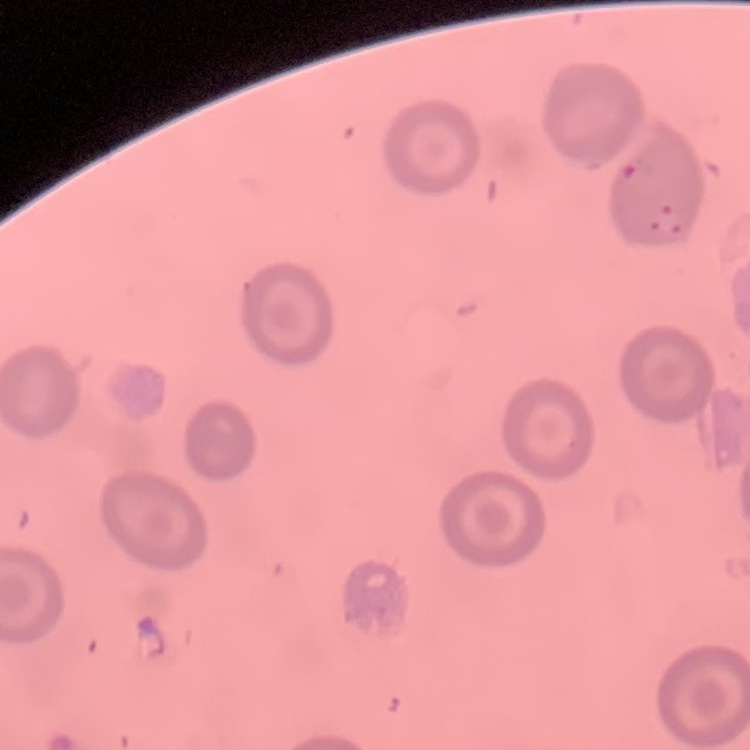
erythrocyte morphology = no rouleaux formation
stain = Field's or Giemsa
preparation = thin peripheral smear
image type = square crop of a larger photomicrograph